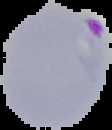
Summary:
  - Image size: 112×130 pixels
  - Preparation: thin blood smear
  - Malaria status: parasitized
  - Image type: cell region segmented out of the field of view; surrounding area masked to black